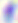 Captured at 400x magnification. Micrograph. Toxoplasma gondii is shown.